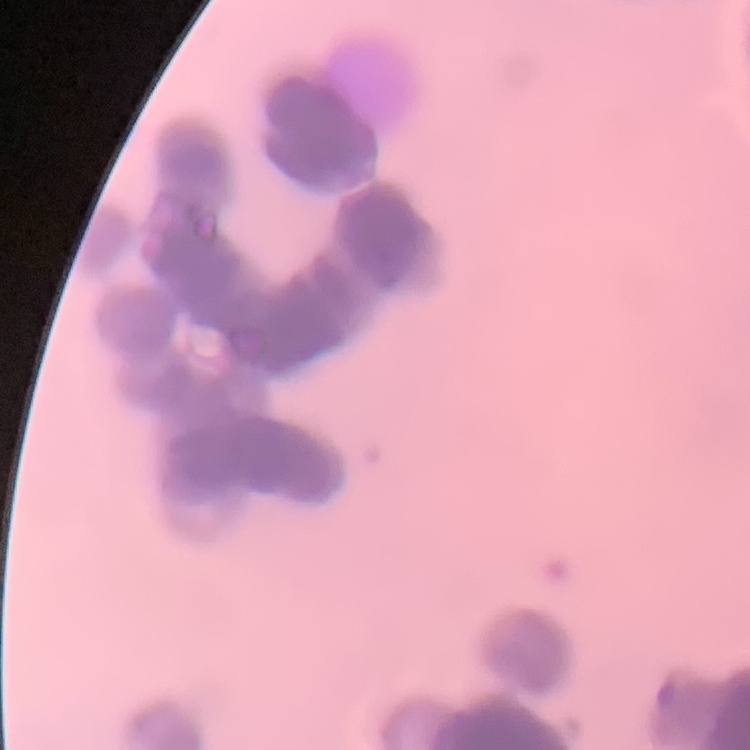

Summary:
  - Red blood cell morphology: rouleaux formation
  - Image type: one tile cut from a larger photomicrograph
  - Stain: Field's or Giemsa
  - Preparation: thin blood film